Classify this cell by malaria status.
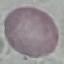
Uninfected.

Photographed with a smartphone camera at the microscope eyepiece. Thin smear of blood. Automatically extracted cell patch, resized to 64 × 64 pixels. Giemsa-stained preparation.